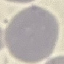 Result: no malaria parasites seen. Automatically extracted cell patch, resized to 64 × 64 pixels. Acquired by smartphone through the microscope eyepiece. Thin blood smear. Giemsa-stained preparation.